Name the blood parasite species.
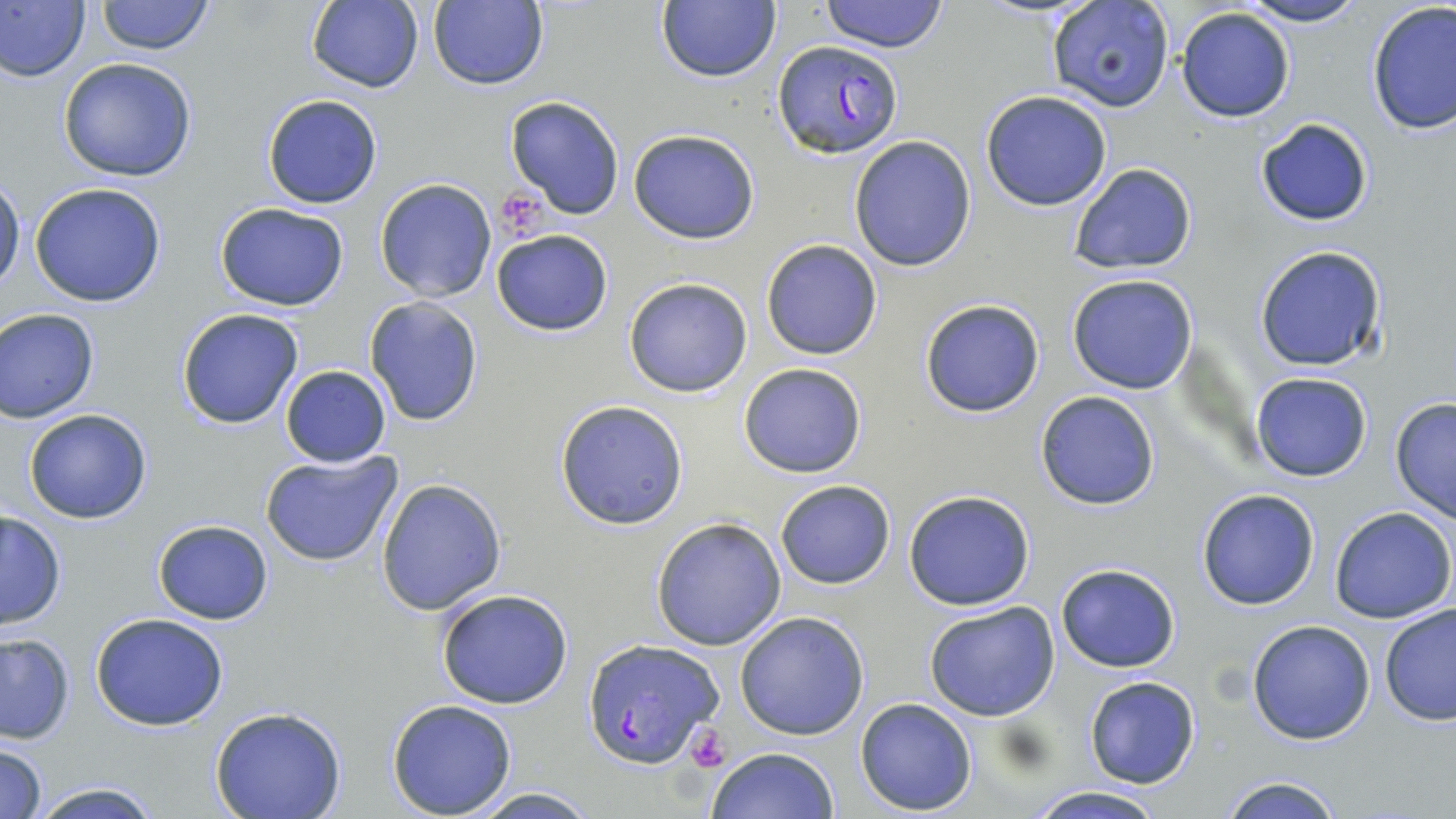
Plasmodium falciparum.

Approximate bounding boxes as [x1, y1, x2, y2] in pixels. Platelet locations: [493, 189, 549, 239], [684, 724, 731, 773]. Uninfected red blood cell locations: [0, 0, 91, 84], [94, 0, 216, 55], [304, 0, 425, 94], [657, 0, 781, 83], [819, 0, 949, 53], [1237, 0, 1368, 27], [426, 1, 550, 90], [1046, 3, 1175, 113], [1364, 3, 1456, 136], [1175, 7, 1295, 124], [57, 57, 197, 182], [982, 92, 1112, 210], [262, 94, 381, 208], [506, 96, 625, 219], [1256, 117, 1374, 227], [627, 128, 761, 244], [848, 135, 977, 271], [1068, 163, 1197, 274], [0, 177, 24, 292], [373, 178, 497, 302], [28, 182, 167, 308], [214, 203, 350, 311], [491, 229, 614, 336], [760, 239, 883, 360], [1253, 244, 1388, 373], [1066, 273, 1198, 394], [622, 276, 754, 398], [364, 296, 483, 426], [917, 298, 1045, 419], [176, 308, 305, 430], [1, 309, 100, 422], [737, 362, 868, 479], [281, 364, 391, 467], [1249, 371, 1373, 482], [1034, 389, 1161, 511], [1389, 396, 1456, 523], [554, 400, 689, 530], [22, 408, 153, 524], [260, 450, 406, 568], [376, 478, 507, 617], [774, 479, 896, 589], [1196, 489, 1321, 610], [903, 490, 1036, 610], [1329, 506, 1456, 624], [0, 510, 67, 630], [650, 516, 788, 651], [153, 519, 274, 624], [1054, 563, 1181, 673], [436, 588, 575, 709], [924, 601, 1063, 721], [1378, 603, 1456, 727], [735, 611, 870, 741], [92, 612, 229, 731], [1247, 619, 1376, 746], [0, 634, 75, 743], [1084, 676, 1201, 788], [854, 697, 978, 815], [386, 698, 518, 817], [209, 708, 348, 819], [0, 741, 48, 819], [708, 747, 838, 819], [1215, 775, 1351, 819], [24, 781, 168, 819], [464, 786, 604, 818], [1024, 786, 1170, 819]. Plasmodium falciparum-infected red blood cell locations: [773, 42, 905, 160], [584, 639, 721, 769]. 1000x magnification. Optical microscopy. May-Grünwald-Giemsa-stained preparation. Thin blood smear. Single field of view. Image is 1456×819 pixels.